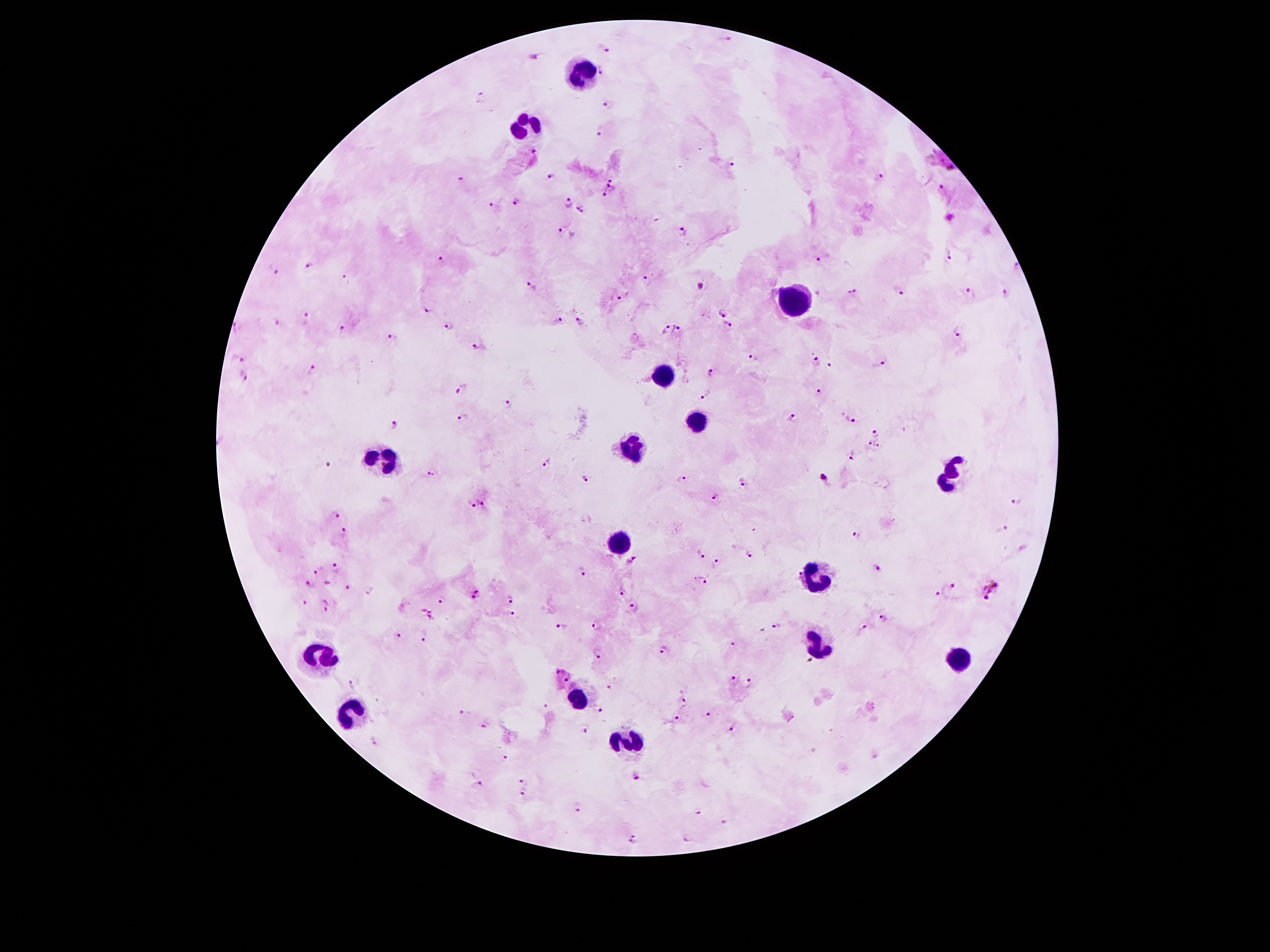

coordinate format = approximate centers as [x, y] in pixels
leukocyte locations = [583, 70], [527, 130], [791, 302], [661, 374], [695, 424], [631, 446], [381, 456], [949, 476], [617, 544], [811, 578], [817, 646], [321, 658], [957, 662], [579, 698], [355, 714], [627, 742]
malaria parasite locations = [725, 39], [603, 48], [603, 70], [481, 97], [608, 106], [600, 134], [535, 152], [731, 166], [550, 177], [878, 177], [462, 179], [612, 179], [610, 187], [939, 187], [604, 197], [516, 202], [492, 205], [568, 205], [582, 210], [562, 231], [684, 234], [950, 259], [817, 260], [439, 262], [1017, 265], [309, 267], [276, 272], [348, 278], [647, 281], [531, 288], [701, 289], [852, 292], [1005, 292], [899, 293], [970, 295], [622, 297], [427, 312], [720, 314], [307, 317], [558, 321], [580, 323], [278, 324], [729, 325], [450, 326], [666, 329], [236, 330], [339, 330], [675, 330], [958, 332], [390, 337], [478, 346], [752, 358], [238, 359], [815, 361], [880, 361], [829, 366], [311, 369], [711, 372], [243, 373], [463, 387], [817, 394], [705, 396], [507, 405], [462, 419], [792, 419], [851, 422], [394, 426], [879, 433], [869, 442], [878, 446], [854, 455], [548, 464], [430, 473], [824, 479], [585, 480], [682, 480], [741, 484], [714, 498], [1017, 502], [473, 503], [485, 503], [335, 515], [1000, 528], [344, 529], [856, 534], [701, 554], [748, 556], [632, 559], [715, 565], [877, 566], [320, 568], [335, 568], [580, 573], [701, 581], [310, 584], [348, 586], [952, 586], [992, 588], [470, 591], [622, 592], [937, 594], [443, 598], [509, 599], [305, 602], [326, 605], [631, 607], [510, 613], [883, 620], [561, 624], [595, 626], [778, 627], [398, 637], [423, 638], [732, 643], [664, 651], [597, 654], [731, 679], [353, 684], [751, 684], [684, 701], [544, 706], [599, 709], [465, 713], [709, 715], [676, 720], [486, 724], [730, 728], [587, 729], [375, 743], [505, 757], [635, 778], [523, 781], [478, 785], [521, 792], [578, 808], [699, 814], [723, 822], [634, 839], [688, 839]
stain = Giemsa
preparation = thick peripheral-blood smear
field of view = one from this slide
magnification = 100x
patient malaria status = infected with Plasmodium falciparum
image size = 1270×952 pixels
capture = smartphone through the microscope eyepiece